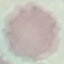 Result: negative for malaria parasites. Giemsa-stained preparation. Cell patch, automatically extracted from a larger field of view and resized to 64 × 64 pixels. Photographed with a smartphone camera at the microscope eyepiece. Thin smear of blood.